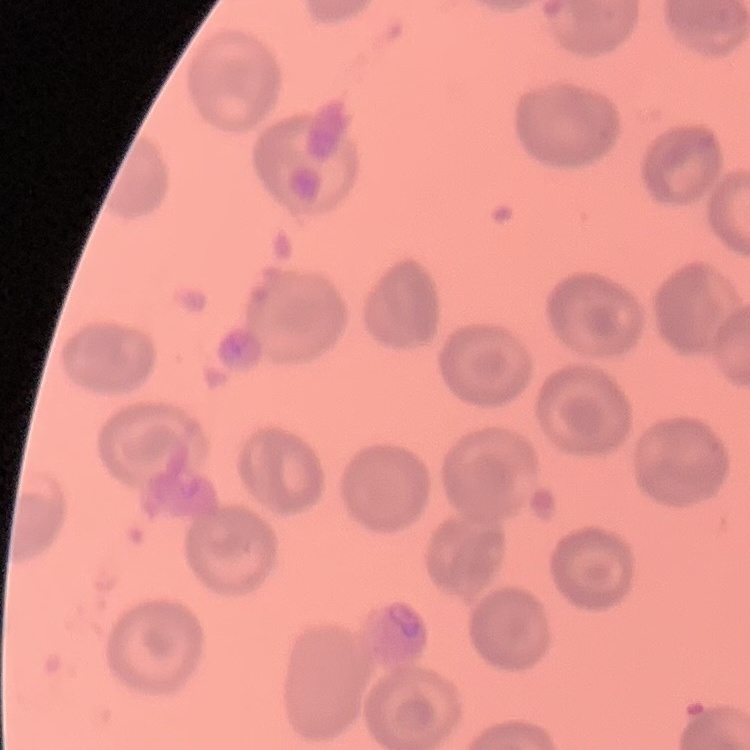

The red blood cells show no rouleaux formation. Thin peripheral smear. Square crop of a larger photomicrograph. Stained with either Field's or Giemsa.